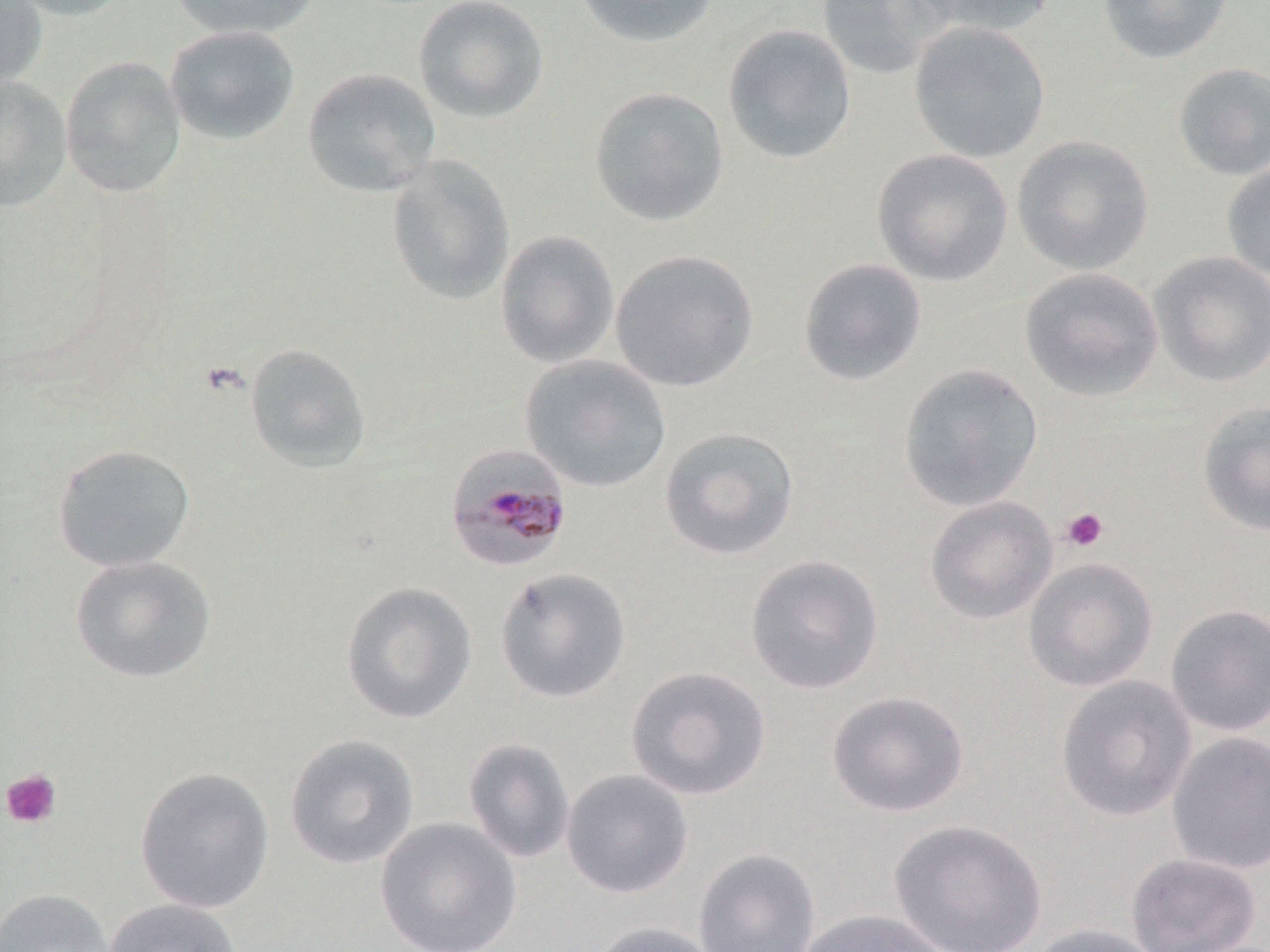 Approximate bounding boxes as (x1, y1, x2, y2) in pixels. Plasmodium malariae-infected red blood cell locations: (445, 442, 573, 573). Platelet locations: (1061, 508, 1108, 552), (1, 768, 62, 829). Uninfected red blood cell locations: (0, 0, 48, 91), (3, 0, 133, 21), (169, 0, 321, 42), (412, 0, 550, 125), (574, 0, 719, 49), (816, 0, 955, 79), (913, 0, 1057, 39), (1097, 0, 1233, 65), (908, 22, 1051, 163), (722, 23, 858, 166), (164, 25, 301, 146), (59, 56, 187, 198), (1171, 61, 1270, 181), (301, 67, 442, 198), (0, 77, 72, 213), (588, 86, 730, 227), (1011, 135, 1155, 276), (871, 148, 1014, 287), (384, 154, 515, 306), (1221, 161, 1270, 281), (495, 229, 620, 369), (609, 249, 760, 393), (1147, 250, 1270, 388), (797, 257, 928, 387), (1019, 267, 1164, 402), (243, 343, 372, 473), (519, 354, 671, 493), (896, 362, 1044, 512), (1197, 400, 1270, 537), (659, 426, 800, 561), (51, 443, 197, 573), (924, 496, 1058, 624), (69, 554, 217, 684), (744, 554, 884, 695), (1023, 556, 1158, 692), (494, 567, 631, 703), (340, 581, 478, 725), (1164, 603, 1270, 737), (625, 666, 772, 800), (1056, 675, 1197, 822), (827, 690, 970, 818), (1167, 732, 1270, 875), (284, 733, 420, 870), (463, 737, 576, 864), (133, 765, 275, 914), (561, 769, 694, 898), (374, 816, 523, 952), (889, 819, 1048, 952), (693, 848, 821, 952), (1126, 853, 1262, 952), (0, 888, 114, 952), (104, 897, 242, 952), (796, 908, 948, 952), (588, 920, 722, 952), (1027, 922, 1164, 952). Slide-level diagnosis: Plasmodium malariae. One field of a larger specimen. 1000x magnification. Light microscopy. Image is 1270×952 pixels. May-Grünwald-Giemsa-stained preparation. Thin blood smear.